Classify this cell by malaria status.
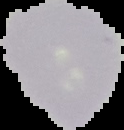

Uninfected.

image size = 124×130 pixels
image type = segmented cell region with the area outside set to black
preparation = thin blood smear